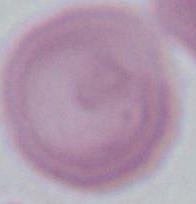

{
  "identification": "erythrocyte",
  "magnification": "1000x",
  "modality": "micrograph"
}